Report the malaria status of this cell.
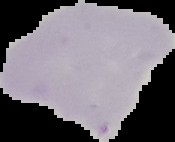
Uninfected.

Summary:
  - Preparation: thin blood smear
  - Image type: segmented cell region on a black background
  - Image size: 175×142 pixels